Classify this cell by malaria status.
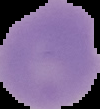
Uninfected.

Summary:
  - Image type: cell region segmented out of the field of view; surrounding area masked to black
  - Preparation: thin blood smear
  - Image size: 100×109 pixels